Comment on the morphology of the red blood cells.
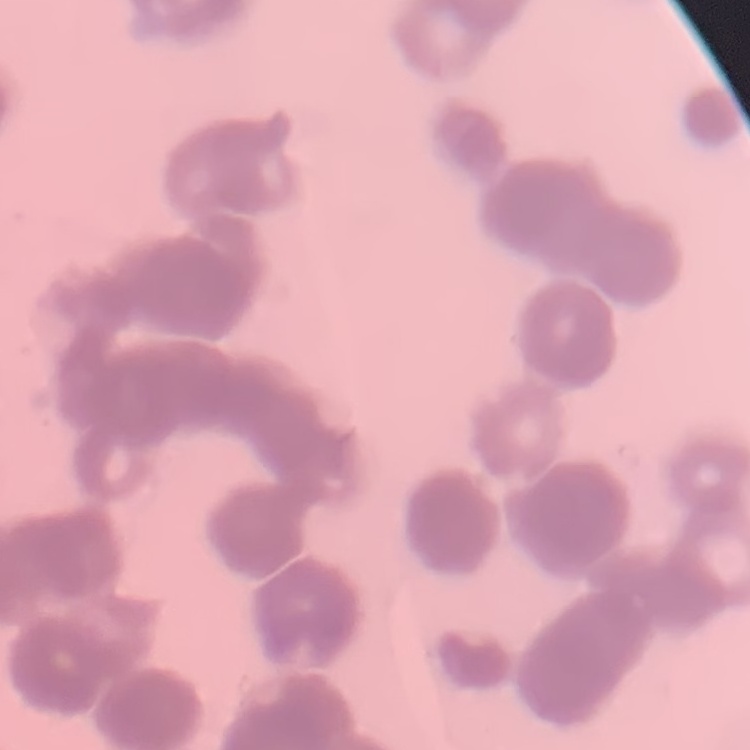

They show rouleaux formation.

Stained with either Field's or Giemsa. Thin blood smear. Square crop of a larger photomicrograph.